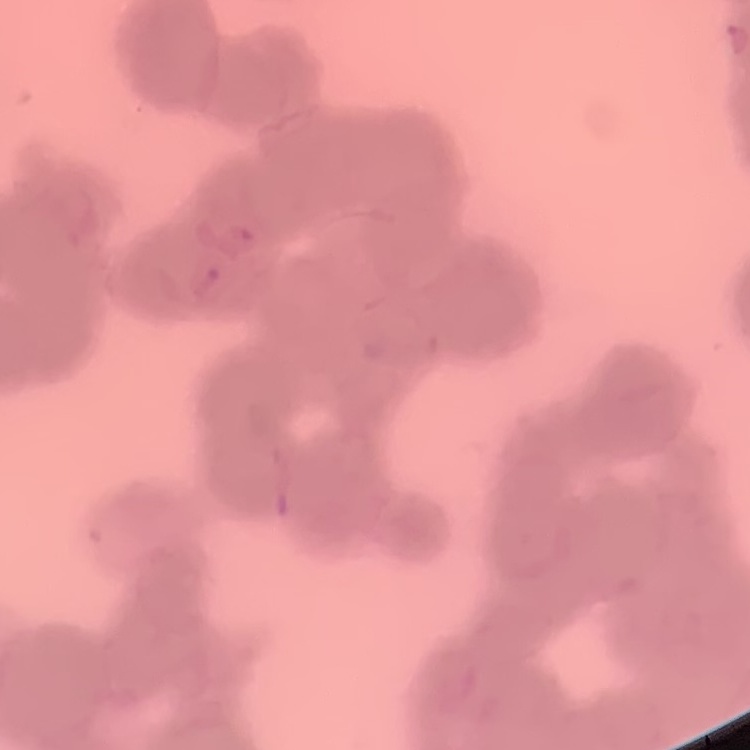
red blood cell morphology = rouleaux formation
stain = Field's or Giemsa
preparation = thin blood smear
image type = square crop of a larger photomicrograph